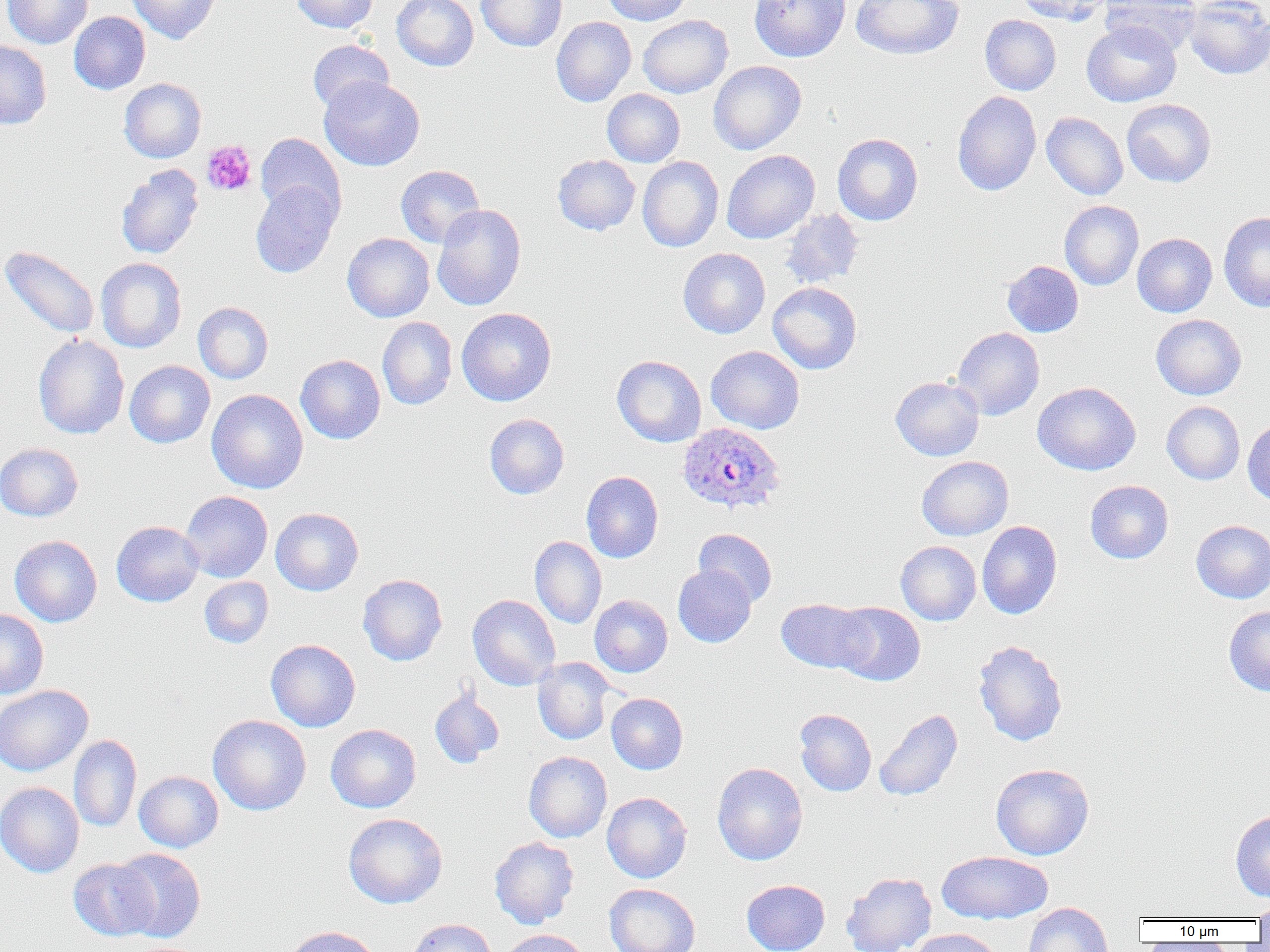

{
  "slide_level_diagnosis": "Plasmodium ovale",
  "platelet_locations": "approximate bounding boxes as (x1,y1)-(x2,y2) corner pairs in pixels: (201,140)-(257,196)",
  "modality": "light microscopy",
  "uninfected_red_blood_cell_locations": "approximate bounding boxes as (x1,y1)-(x2,y2) corner pairs in pixels: (2,0)-(92,49), (126,0)-(221,44), (291,0)-(378,34), (392,0)-(478,71), (475,0)-(567,52), (602,0)-(692,26), (750,0)-(850,62), (851,0)-(964,60), (1015,0)-(1109,24), (1100,0)-(1201,55), (1184,0)-(1270,80), (69,12)-(150,94), (638,15)-(733,98), (980,15)-(1061,95), (551,16)-(636,106), (1081,21)-(1181,107), (0,40)-(52,129), (307,40)-(394,114), (709,60)-(806,154), (319,76)-(425,171), (119,78)-(206,163), (602,89)-(685,167), (952,91)-(1041,196), (1121,99)-(1216,187), (1041,112)-(1128,200), (255,133)-(346,224), (832,133)-(923,226), (721,150)-(820,244), (553,155)-(640,235), (638,156)-(724,252), (116,164)-(204,260), (395,165)-(485,248), (250,181)-(341,278), (1059,200)-(1144,290), (432,204)-(526,311), (779,209)-(864,289), (1218,211)-(1270,312), (343,233)-(434,322), (1132,233)-(1217,317), (1,245)-(100,339), (678,248)-(770,338), (95,258)-(187,353), (1002,260)-(1083,337), (768,282)-(862,374), (193,302)-(273,383), (456,307)-(556,406), (1151,314)-(1246,400), (377,317)-(457,410), (952,327)-(1044,420), (33,334)-(129,439), (706,346)-(804,434), (295,355)-(385,444), (612,355)-(706,447), (124,360)-(215,448), (890,375)-(984,461), (1033,381)-(1141,475), (206,389)-(308,494), (1162,401)-(1245,485), (484,414)-(569,499), (1242,419)-(1270,505), (0,443)-(83,521), (916,456)-(1013,540), (581,471)-(663,563), (1085,480)-(1173,563), (180,491)-(273,582), (270,507)-(363,596), (1191,520)-(1270,603), (111,521)-(204,607), (977,521)-(1062,619), (694,528)-(777,607), (10,535)-(102,627), (530,535)-(607,628), (896,541)-(981,625), (673,564)-(756,647), (358,574)-(447,666), (199,576)-(273,648), (467,594)-(560,691), (590,595)-(672,677), (776,598)-(872,673), (831,602)-(925,686), (1224,606)-(1270,696), (0,609)-(49,699), (266,639)-(360,732), (973,639)-(1068,746), (533,657)-(616,744), (0,685)-(93,776), (429,689)-(504,769), (606,693)-(688,774), (794,709)-(877,796), (874,709)-(962,801), (208,715)-(311,815), (326,724)-(421,813), (69,734)-(141,833), (524,751)-(612,842), (711,762)-(807,866), (990,763)-(1094,860), (134,771)-(223,853), (0,781)-(85,877), (602,792)-(692,883), (1230,809)-(1270,901), (343,813)-(447,908), (489,836)-(579,929), (113,849)-(206,942), (937,850)-(1053,924), (68,858)-(158,941), (842,872)-(936,952), (741,879)-(830,952), (604,883)-(700,952), (1249,901)-(1269,923), (1023,902)-(1112,952), (407,918)-(497,952), (284,925)-(381,952), (909,928)-(1002,952), (499,929)-(591,952)",
  "field_of_view": "one of a larger specimen",
  "image_size": "1270×952 pixels",
  "magnification": "1000x",
  "plasmodium_ovale_infected_red_blood_cell_locations": "approximate bounding boxes as (x1,y1)-(x2,y2) corner pairs in pixels: (678,421)-(785,515)",
  "preparation": "thin blood film"
}